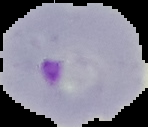

Summary:
  - Preparation: thin blood smear
  - Image size: 148×127 pixels
  - Image type: segmented cell region on a black background
  - Malaria status: parasitized